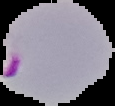
Summary:
  - Preparation: thin blood film
  - Malaria status: parasitized
  - Image type: segmented cell region with the area outside set to black
  - Image size: 115×106 pixels